Give the preparation type.
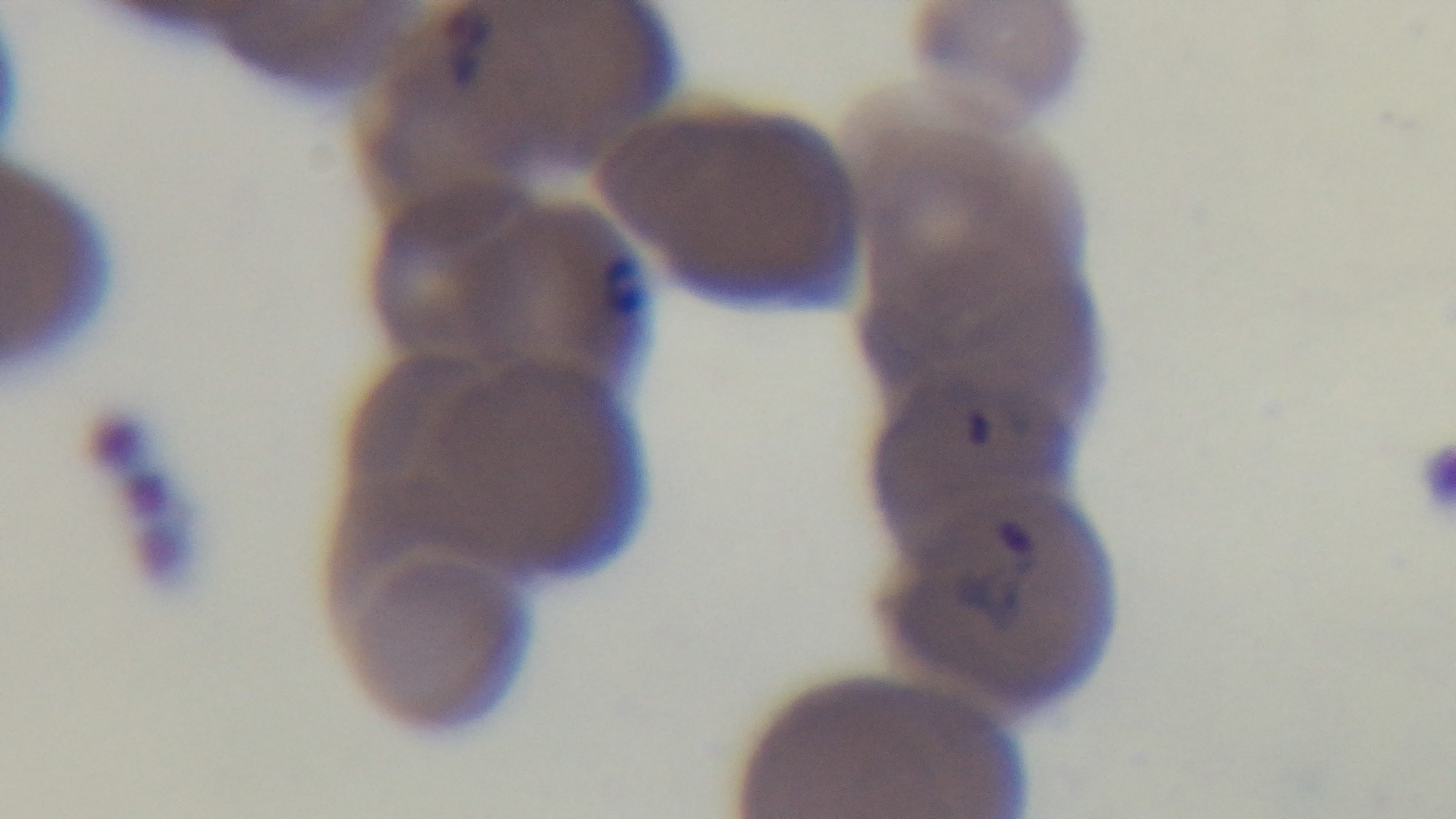

A thin smear.

Light microscopy. Oil-immersion objective, 100x. Captured with a mounted 4K digital camera. Malaria status: positive. Giemsa stain. One field from the slide.